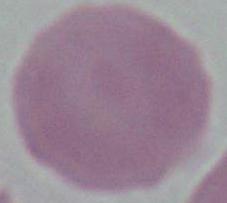

Summary:
  - Modality: photomicrograph
  - Magnification: 1000x
  - Identification: erythrocyte